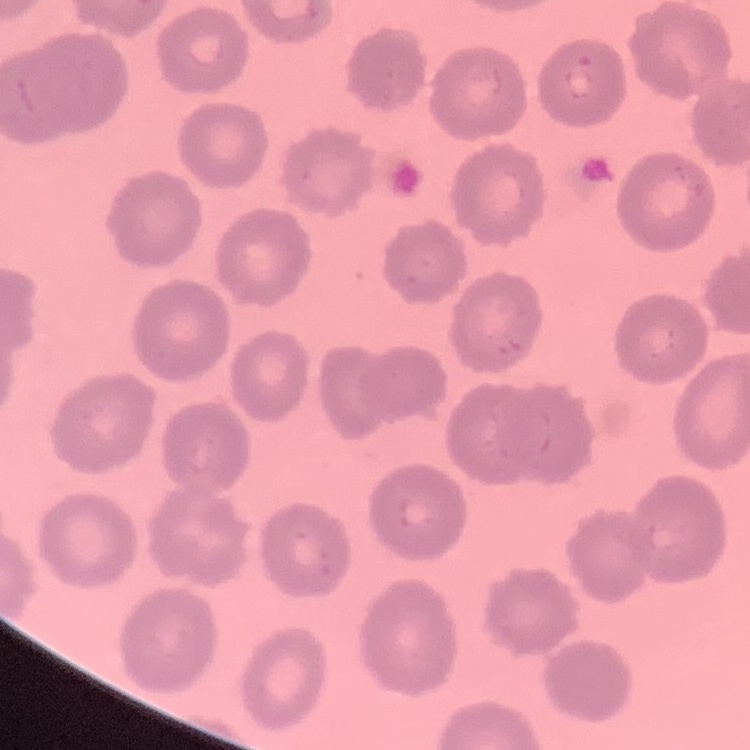 The erythrocytes show no rouleaux formation. One tile cut from a larger photomicrograph. Thin blood film. Stained with either Field's or Giemsa.